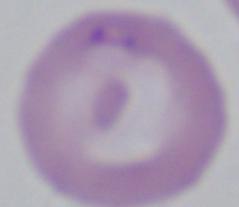

Summary:
  - Modality: micrograph
  - Identification: Babesia
  - Magnification: 1000x